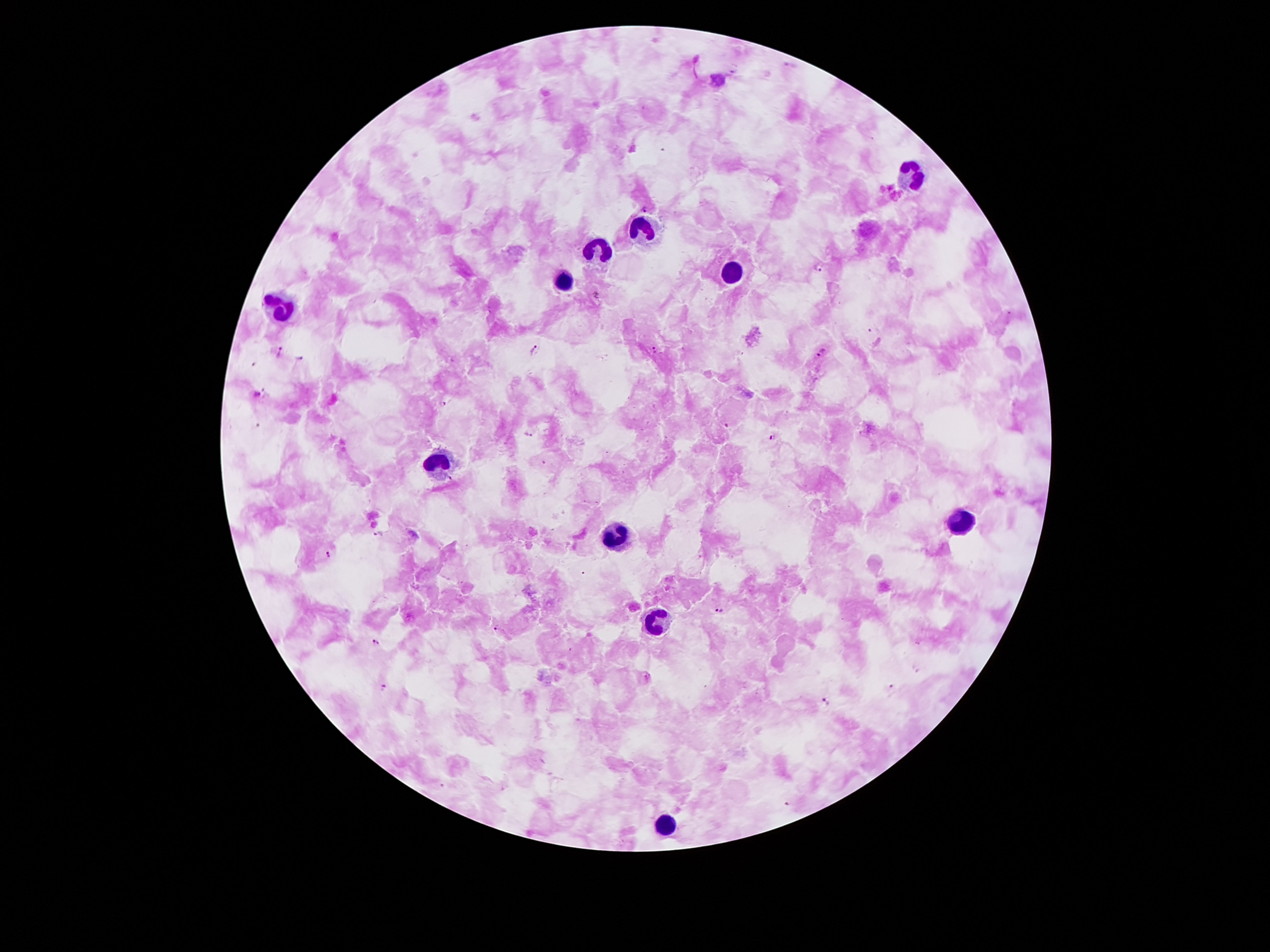 Approximate centers as [x, y] in pixels. Plasmodium parasite locations: [646, 208], [819, 267], [596, 294], [654, 348], [532, 349], [823, 351], [281, 352], [259, 395], [441, 405], [728, 425], [530, 436], [774, 437], [451, 479], [379, 535], [329, 555], [719, 610], [496, 629], [375, 643], [892, 687], [383, 688], [827, 702]. Leukocyte locations: [909, 174], [645, 227], [601, 246], [731, 273], [561, 277], [281, 308], [437, 459], [964, 521], [615, 535], [657, 622], [664, 823]. Thick blood film. One field from this slide. Smartphone photograph taken through the microscope eyepiece. Giemsa-stained preparation. Patient malaria status: positive for Plasmodium falciparum. 100x magnification. Image is 1270×952 pixels.